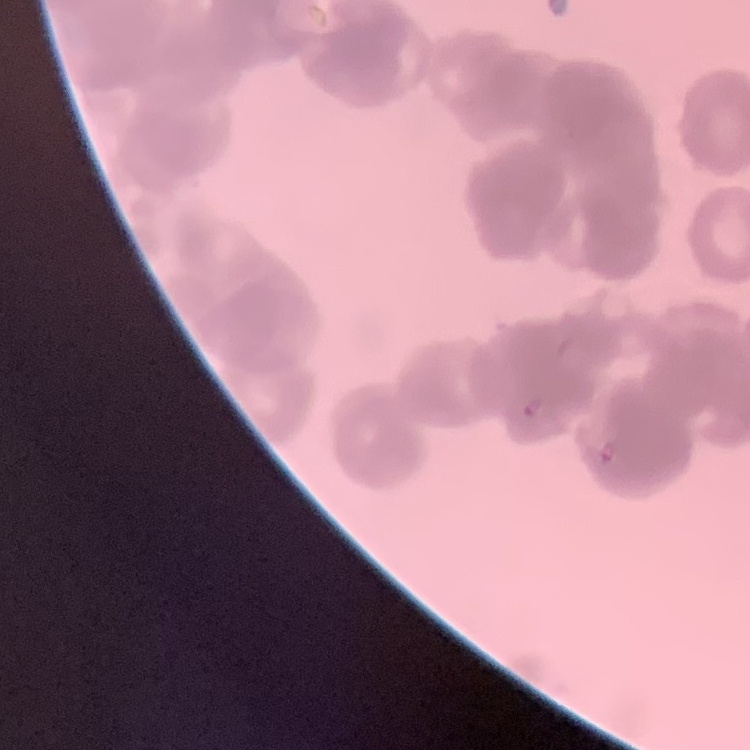

Summary:
  - Red blood cell morphology: rouleaux formation
  - Preparation: thin blood smear
  - Stain: Field's or Giemsa
  - Image type: square crop of a larger photomicrograph